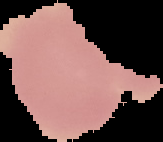

image size = 163×142 pixels
malaria status = uninfected
preparation = thin blood film
image type = segmented cell region on a black background